Assess this cell for malaria.
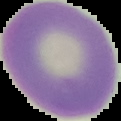

Uninfected.

Image is 121×121 pixels. From a thin blood film. Segmented cell region on a black background.